Comment on the morphology of the red blood cells.
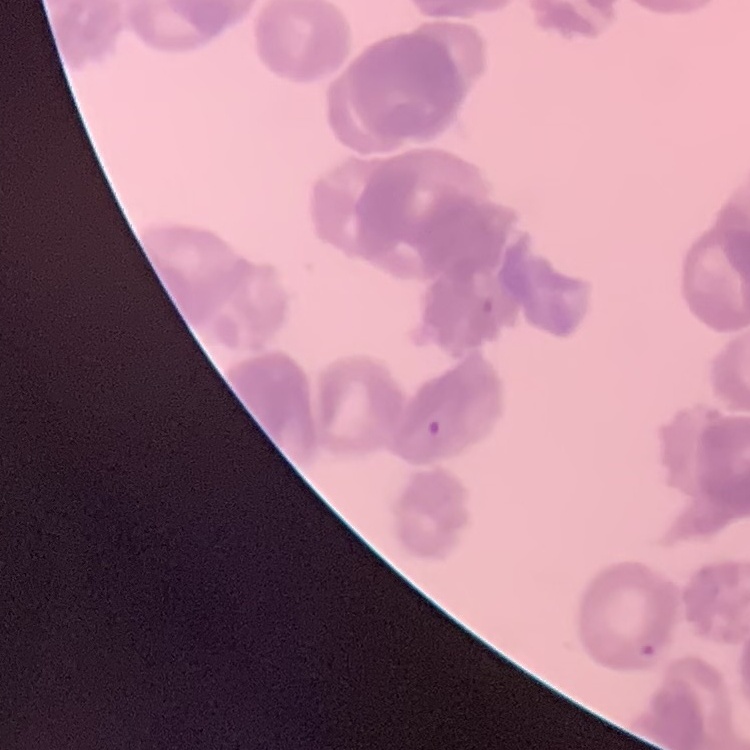
Rouleaux formation.

Thin peripheral smear. Field's or Giemsa stain. Square crop of a larger photomicrograph.